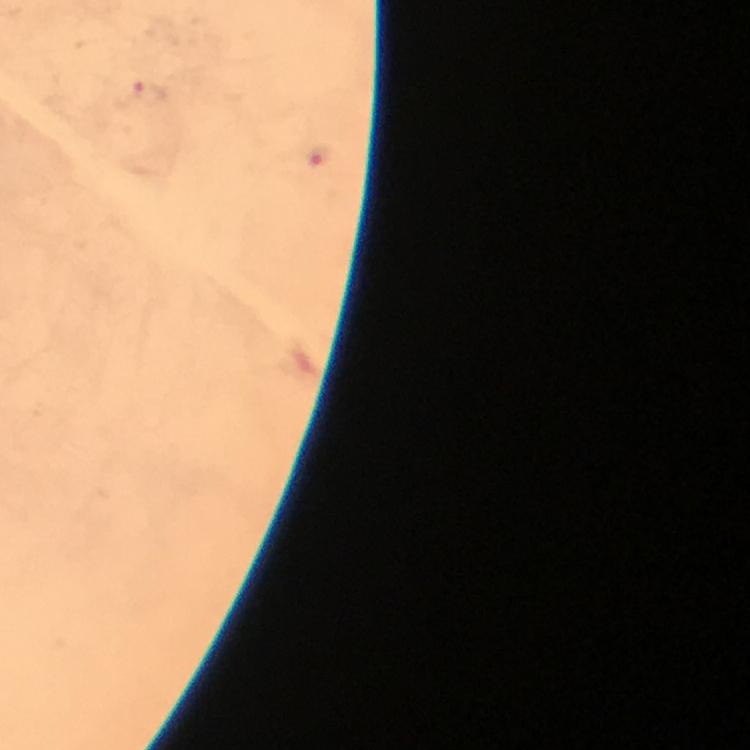
Approximate object centers, in pixels from the top-left corner. Malaria parasite locations: (x=148, y=91), (x=321, y=156). Giemsa-stained preparation. Thick blood smear. Image is 750×750 pixels. At 100x magnification. From a malaria diagnostic workup. Cropped region of a single field of view. Photographed through the microscope with a smartphone camera. Immersion oil applied.